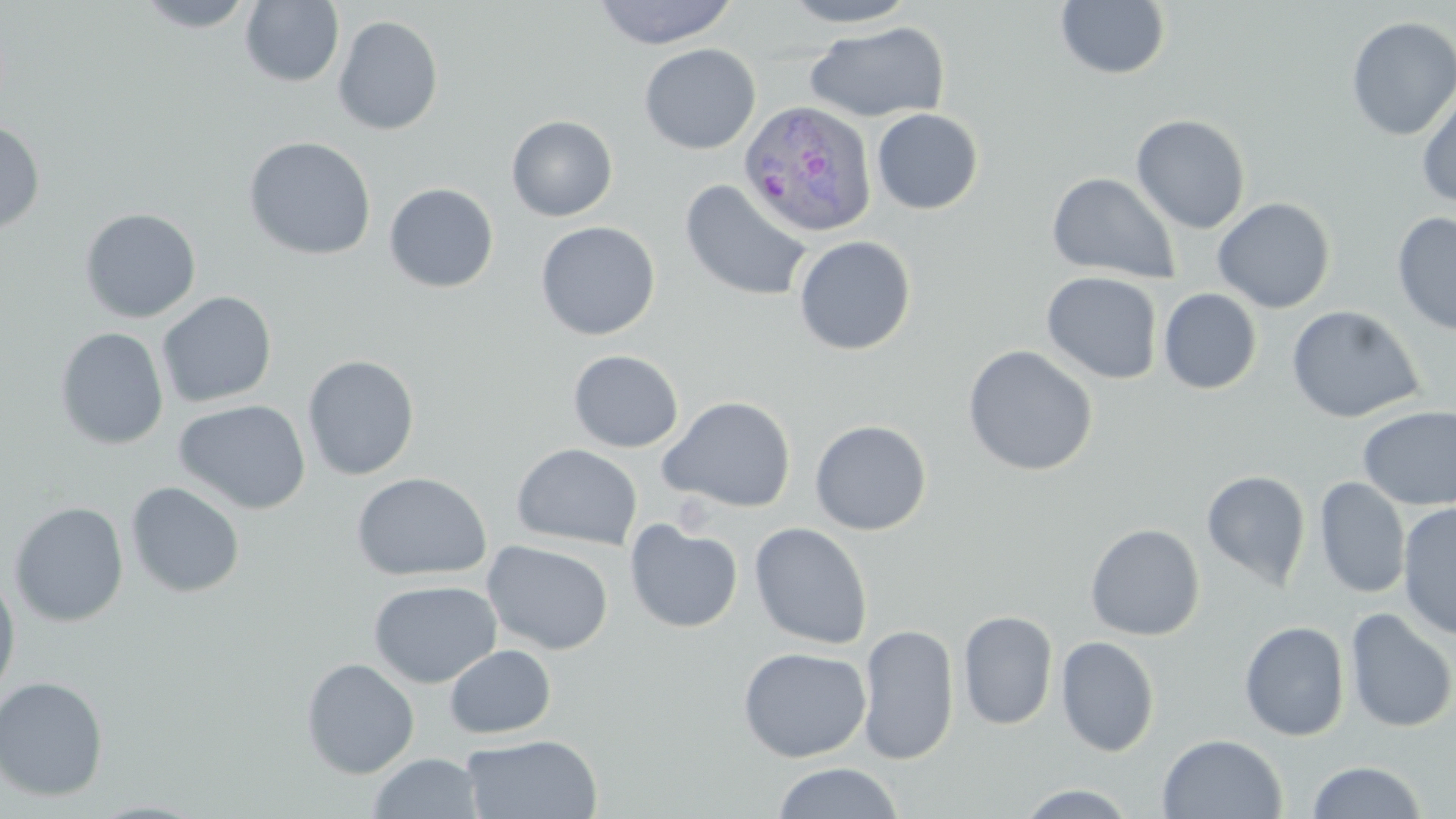

Approximate bounding boxes as (x1,y1)-(x2,y2) corner pairs in pixels. Uninfected red blood cell locations: (134,0)-(257,32), (591,0)-(739,49), (779,0)-(920,28), (240,1)-(344,88), (1056,1)-(1170,80), (333,15)-(444,136), (1345,16)-(1456,141), (805,21)-(950,123), (639,43)-(760,155), (1416,86)-(1456,209), (871,108)-(983,215), (1131,114)-(1251,234), (506,115)-(617,221), (0,119)-(45,235), (243,136)-(377,261), (1047,172)-(1180,283), (679,179)-(814,302), (384,182)-(499,293), (1212,197)-(1336,314), (79,208)-(201,323), (1392,212)-(1456,338), (535,221)-(660,340), (793,235)-(916,356), (1041,272)-(1163,384), (1158,288)-(1262,394), (157,291)-(277,408), (1287,305)-(1424,423), (54,326)-(169,450), (962,344)-(1099,477), (568,350)-(684,453), (301,354)-(420,481), (658,395)-(797,513), (174,399)-(311,515), (1358,405)-(1456,510), (810,420)-(932,535), (511,443)-(643,551), (1201,470)-(1311,589), (351,472)-(492,581), (1314,478)-(1410,599), (126,481)-(245,598), (9,501)-(129,627), (1398,502)-(1456,641), (625,519)-(743,633), (749,522)-(873,650), (1085,522)-(1205,641), (481,540)-(614,655), (0,571)-(21,702), (368,579)-(502,688), (1344,607)-(1456,733), (957,609)-(1058,731), (1239,620)-(1350,741), (957,623)-(1159,740), (858,624)-(959,765), (1056,635)-(1159,757), (444,644)-(556,739), (737,646)-(871,762), (301,657)-(419,779), (0,675)-(109,802), (1157,733)-(1287,819), (461,734)-(603,819), (367,752)-(484,819), (1306,760)-(1428,818), (772,761)-(904,819), (1016,783)-(1140,818). Plasmodium ovale-infected red blood cell locations: (739,100)-(879,241). Slide-level diagnosis: Plasmodium ovale. Thin blood smear. One field of a larger specimen. Image is 1456×819 pixels. Light microscopy. 1000x magnification. May-Grünwald-Giemsa stain.